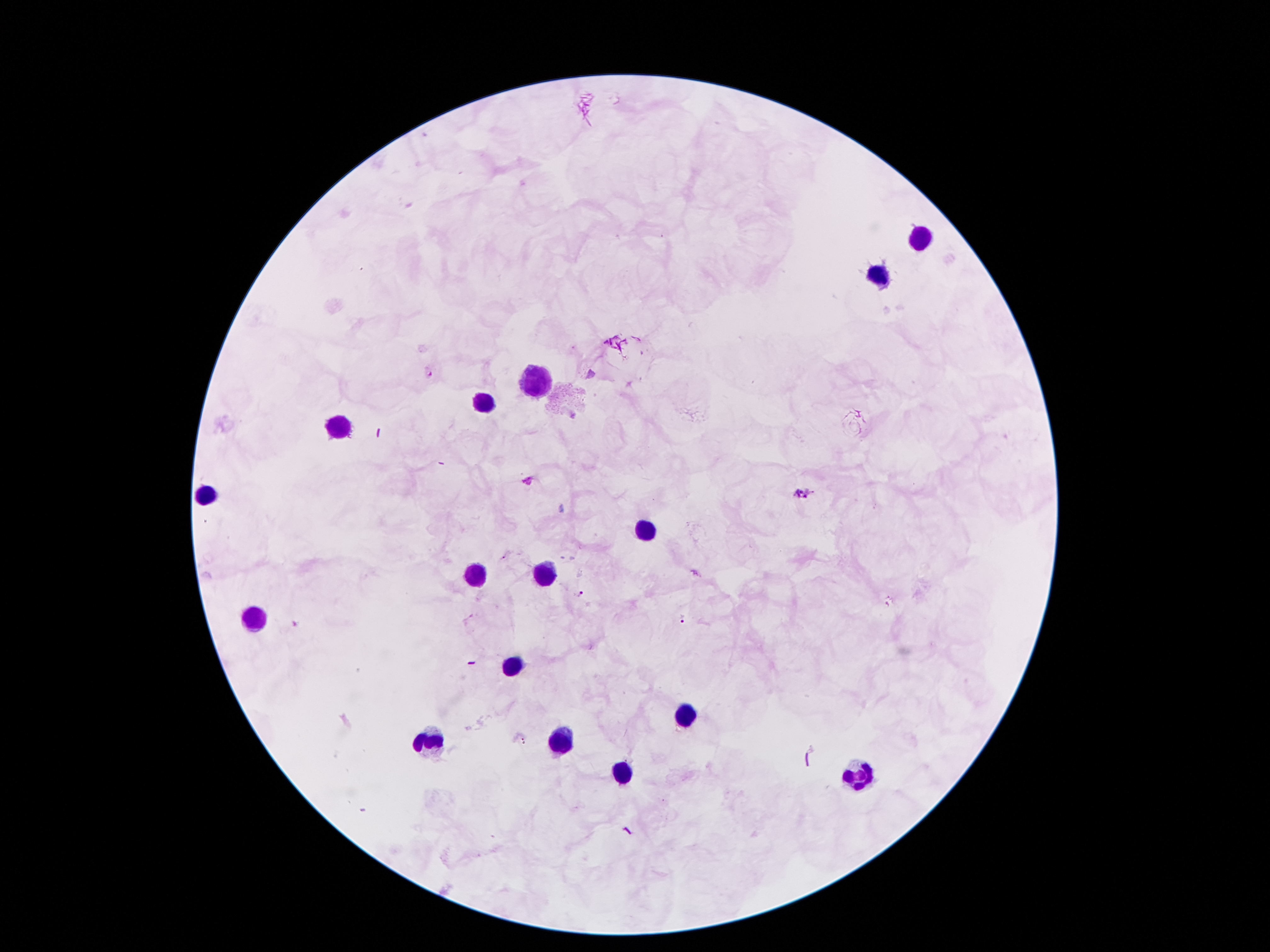
Approximate object centers, in pixels from the top-left corner.
Summary:
  - Plasmodium parasite locations: (x=428, y=372), (x=528, y=480), (x=805, y=491), (x=579, y=593), (x=680, y=619), (x=522, y=741)
  - Leukocyte locations: (x=918, y=241), (x=881, y=274), (x=541, y=381), (x=485, y=403), (x=335, y=429), (x=205, y=498), (x=645, y=536), (x=475, y=573), (x=543, y=575), (x=255, y=618), (x=511, y=668), (x=686, y=716), (x=558, y=741), (x=429, y=743), (x=623, y=771), (x=862, y=776)
  - Stain: Giemsa
  - Capture: smartphone camera through the microscope eyepiece
  - Patient malaria status: positive for Plasmodium falciparum
  - Magnification: 100x
  - Field of view: single
  - Image size: 1270×952 pixels
  - Preparation: thick peripheral-blood smear